Classify this cell by malaria status.
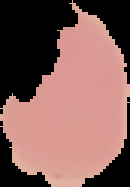

It is uninfected.

image size = 130×187 pixels
image type = segmented cell region with the area outside set to black
preparation = thin blood film